Identify the parasite.
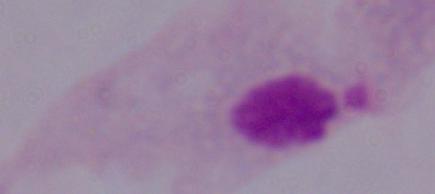

A trichomonad.

{
  "magnification": "1000x",
  "modality": "photomicrograph"
}